Comment on the morphology of the erythrocytes.
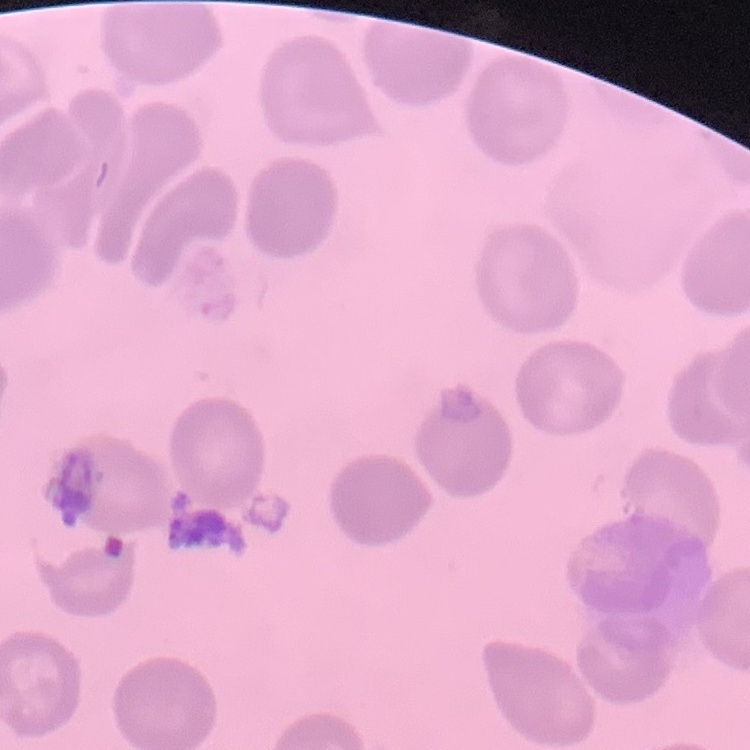
They show no rouleaux formation.

Summary:
  - Preparation: thin peripheral smear
  - Image type: square crop of a larger photomicrograph
  - Stain: Field's or Giemsa